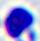
A leukocyte is seen. Captured at 400x magnification. Micrograph.